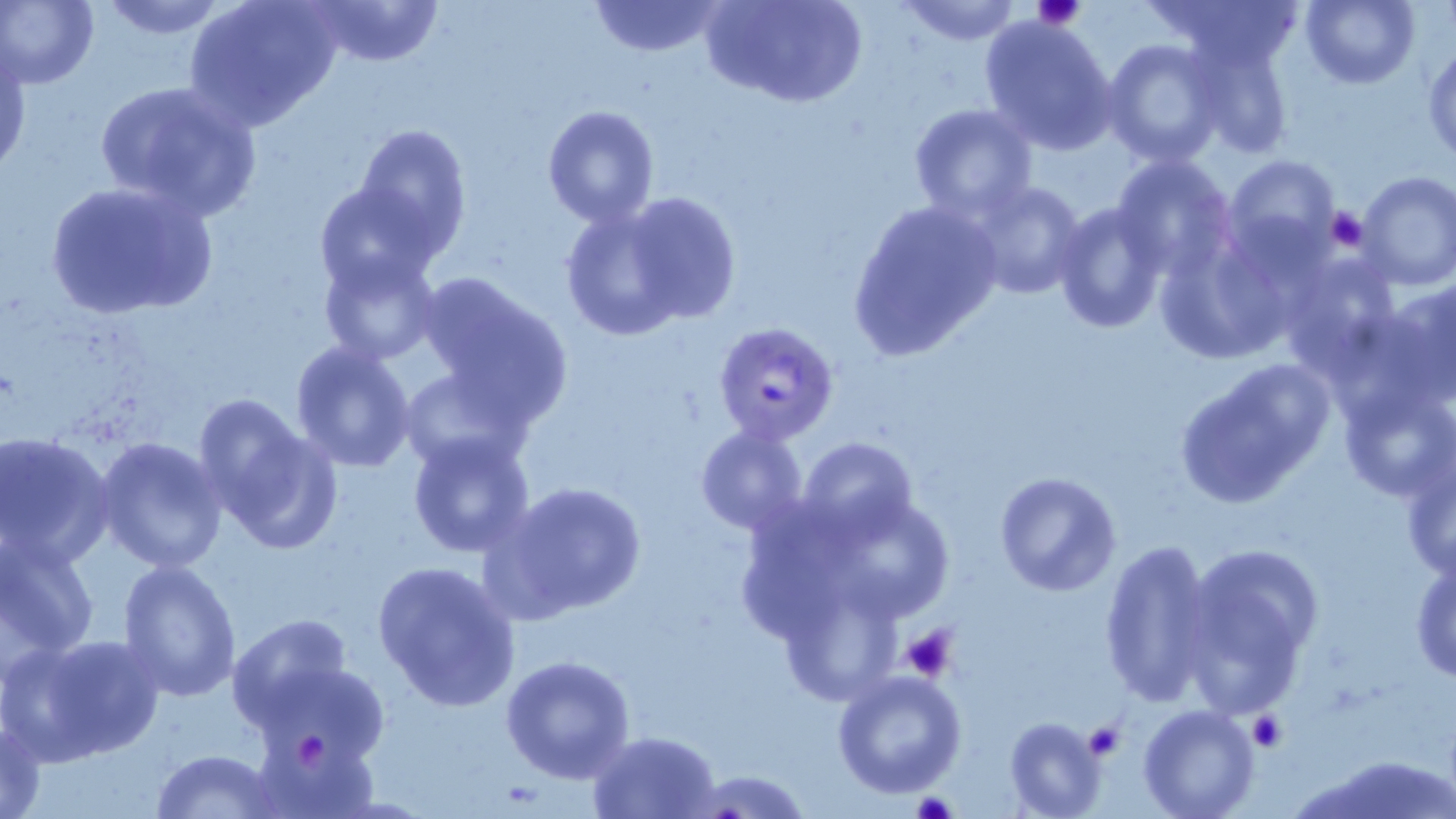

Summary:
  - Coordinate format: approximate bounding boxes as (x1, y1, x2, y2) in pixels
  - Platelet locations: (1033, 0, 1086, 30), (1325, 208, 1370, 251), (901, 626, 957, 681), (1248, 711, 1287, 752), (1082, 723, 1126, 760), (299, 732, 331, 771), (911, 792, 958, 819)
  - Plasmodium falciparum-infected red blood cell locations: (713, 322, 839, 445)
  - Uninfected red blood cell locations: (94, 0, 231, 40), (186, 0, 342, 130), (304, 0, 445, 70), (712, 0, 864, 109), (897, 0, 1024, 46), (1147, 0, 1308, 75), (1301, 0, 1419, 88), (1, 1, 100, 88), (586, 1, 725, 58), (979, 15, 1117, 152), (1187, 33, 1293, 160), (1102, 38, 1225, 167), (1, 40, 30, 176), (1425, 40, 1456, 165), (92, 79, 262, 219), (908, 103, 1037, 221), (542, 104, 660, 227), (351, 123, 472, 255), (1111, 153, 1235, 278), (1224, 156, 1342, 264), (1356, 171, 1456, 292), (965, 178, 1087, 300), (44, 179, 218, 320), (314, 182, 443, 297), (560, 194, 727, 340), (844, 198, 1003, 362), (1053, 201, 1167, 334), (317, 249, 441, 365), (1273, 251, 1404, 376), (409, 273, 573, 431), (1364, 276, 1456, 417), (290, 340, 418, 471), (1171, 359, 1337, 507), (399, 368, 532, 473), (1337, 378, 1454, 502), (200, 402, 337, 551), (695, 424, 810, 535), (406, 430, 536, 558), (1, 434, 114, 569), (96, 436, 228, 573), (797, 436, 917, 544), (1399, 441, 1456, 582), (994, 470, 1121, 596), (495, 479, 648, 619), (0, 534, 100, 660), (1096, 539, 1217, 708), (1175, 543, 1324, 717), (1411, 551, 1456, 684), (116, 557, 242, 703), (370, 559, 522, 712), (226, 613, 355, 732), (17, 633, 167, 764), (500, 654, 636, 783), (250, 660, 391, 768), (831, 669, 967, 798), (1138, 705, 1260, 819), (1, 713, 48, 819), (1005, 716, 1109, 819), (250, 726, 379, 819), (586, 730, 720, 818), (151, 749, 284, 818), (679, 767, 815, 819)
  - Slide-level diagnosis: Plasmodium falciparum
  - Preparation: thin blood film
  - Magnification: 1000x
  - Modality: light microscopy
  - Field of view: single
  - Stain: May-Grünwald-Giemsa
  - Image size: 1456×819 pixels